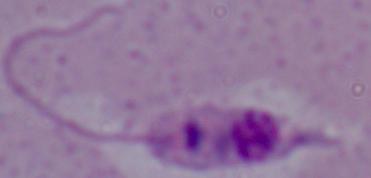

Summary:
  - Magnification: 1000x
  - Identification: Leishmania
  - Modality: micrograph